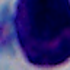

{
  "identification": "leukocyte",
  "magnification": "1000x",
  "modality": "micrograph"
}